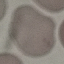
Summary:
  - Result: no malaria parasites detected
  - Image type: automatically extracted cell patch, resized to 64 × 64 pixels
  - Capture: smartphone through the microscope eyepiece
  - Stain: Giemsa
  - Preparation: thin blood smear